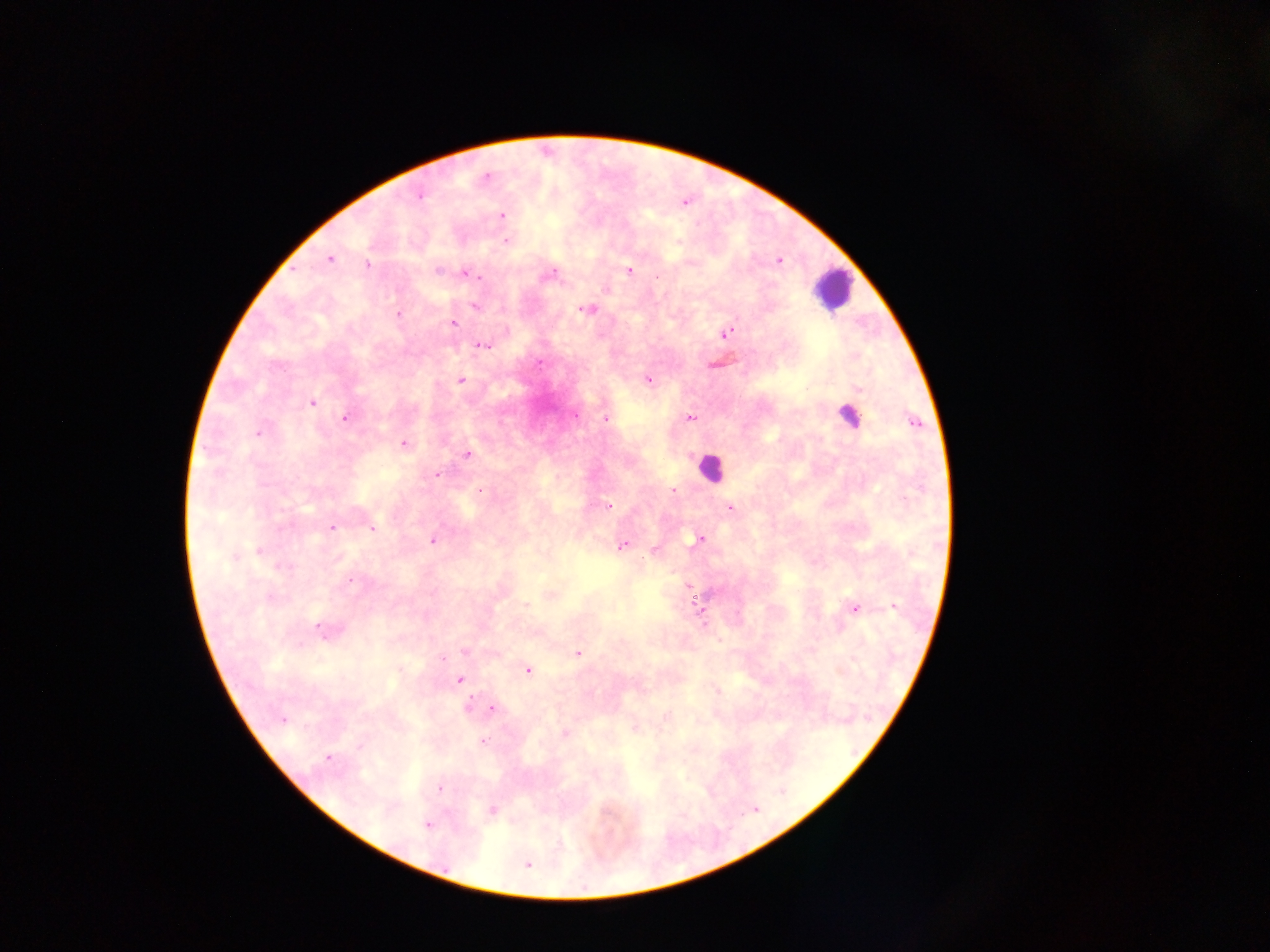

{
  "image_size": "1270×952 pixels",
  "preparation": "thick blood film",
  "capture": "mobile-phone photograph through a microscope",
  "field_of_view": "single",
  "country": "Ghana",
  "malaria_parasite_locations": "approximate centers as {x, y} in pixels: {486, 178}, {420, 194}, {502, 216}, {505, 240}, {329, 258}, {777, 261}, {366, 264}, {438, 269}, {629, 270}, {464, 273}, {550, 274}, {605, 288}, {474, 305}, {584, 309}, {398, 313}, {454, 322}, {726, 333}, {482, 345}, {648, 378}, {460, 379}, {312, 402}, {346, 416}, {575, 416}, {606, 418}, {691, 418}, {914, 422}, {258, 431}, {403, 444}, {465, 455}, {436, 473}, {480, 489}, {672, 489}, {608, 505}, {729, 508}, {332, 527}, {370, 528}, {699, 537}, {433, 540}, {622, 545}, {258, 550}, {654, 550}, {550, 594}, {525, 605}, {854, 607}, {893, 607}, {322, 630}, {465, 651}, {578, 653}, {527, 669}, {459, 679}, {468, 706}, {491, 707}, {282, 718}, {634, 727}, {565, 734}, {482, 740}, {327, 757}, {439, 788}, {492, 810}, {426, 823}, {525, 863}",
  "leukocyte_locations": "approximate centers as {x, y} in pixels: {833, 289}, {847, 413}, {710, 468}"
}